Give the position of every Plasmodium parasite.
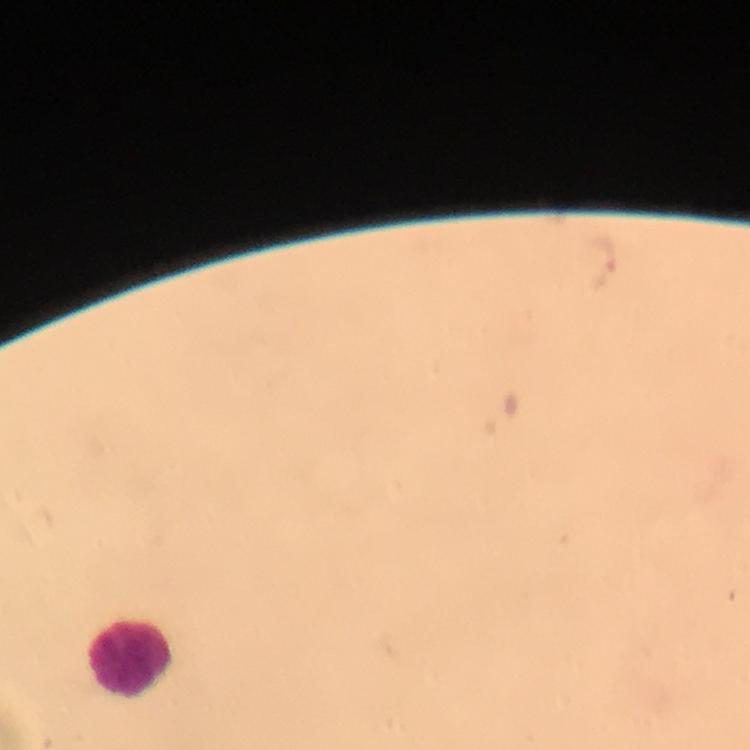

Approximate object centers, in pixels from the top-left corner.
Plasmodium parasites: (x=603, y=260).

Summary:
  - Leukocyte locations: (x=130, y=656)
  - Stain: Giemsa
  - Context: from a malaria diagnostic workup
  - Cropped from: a single field of view
  - Preparation: thick blood smear
  - Image size: 750×750 pixels
  - Immersion oil: applied
  - Magnification: 100x
  - Capture: smartphone photograph through a microscope